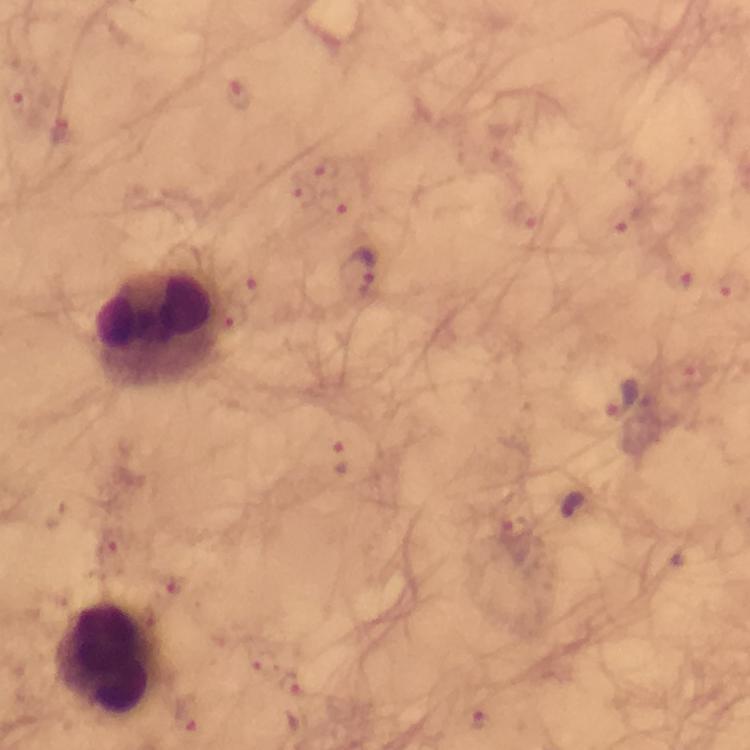

Approximate centers as {x, y} in pixels.
Summary:
  - Plasmodium parasite locations: {237, 94}, {15, 96}, {64, 132}, {332, 171}, {301, 194}, {337, 206}, {525, 215}, {625, 226}, {357, 273}, {680, 278}, {244, 289}, {236, 316}, {693, 376}, {620, 399}, {338, 457}, {514, 528}, {109, 549}, {165, 592}, {263, 665}, {291, 685}, {188, 716}, {477, 716}
  - Leukocyte locations: {157, 330}, {107, 660}
  - Cropped from: a single field of view
  - Context: from a malaria diagnostic workup
  - Capture: smartphone photograph through a microscope
  - Stain: Giemsa
  - Preparation: thick blood smear
  - Magnification: 100x
  - Image size: 750×750 pixels
  - Immersion oil: used